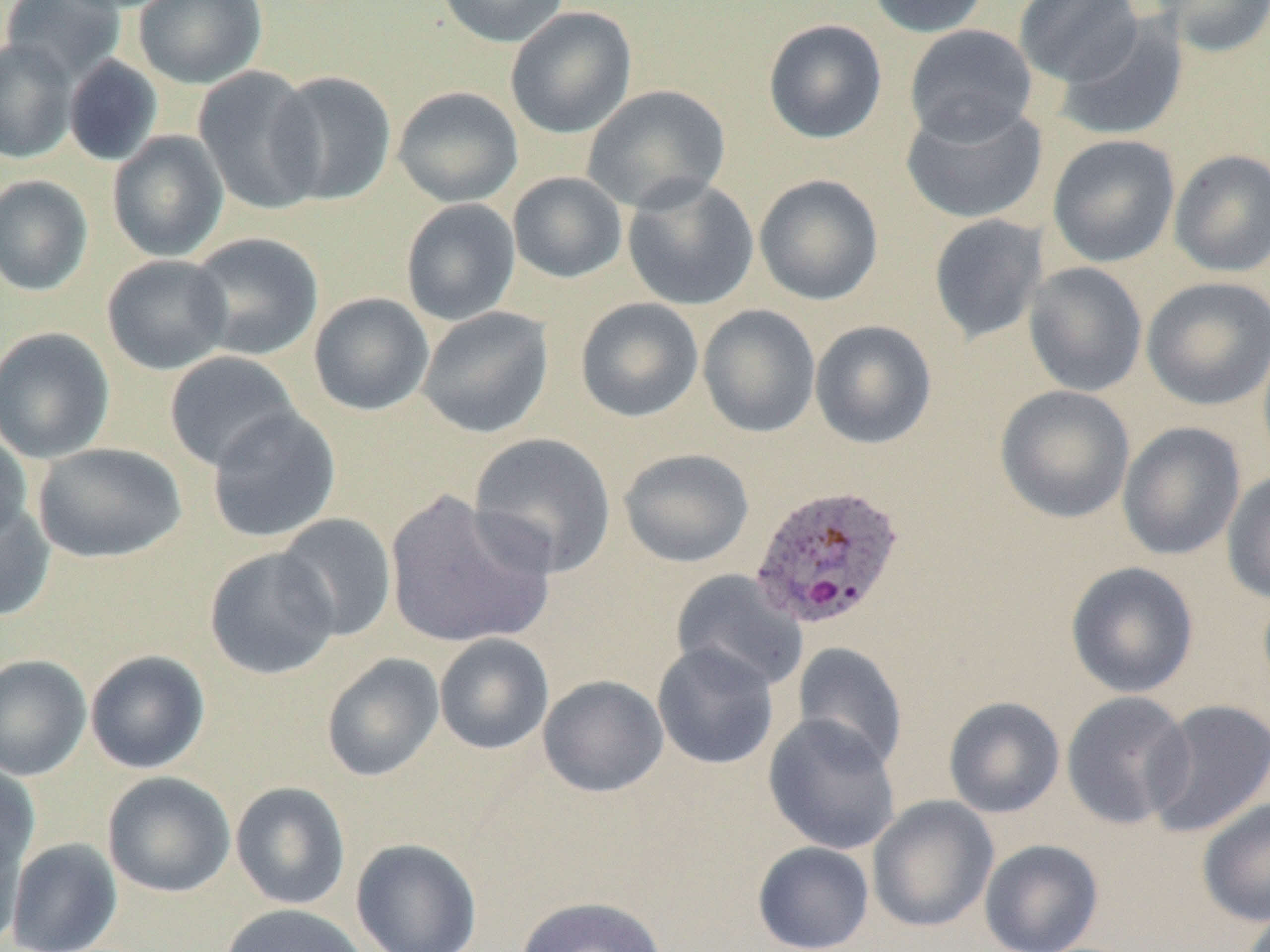
slide-level diagnosis = Plasmodium ovale
field of view = single
Plasmodium ovale-infected red blood cell locations = approximate bounding boxes as named x1/y1/x2/y2 corners in pixels: (x1=749, y1=482, x2=905, y2=632)
modality = light microscopy
magnification = 1000x
uninfected red blood cell locations = approximate bounding boxes as named x1/y1/x2/y2 corners in pixels: (x1=1, y1=0, x2=127, y2=84), (x1=133, y1=0, x2=268, y2=89), (x1=438, y1=0, x2=570, y2=48), (x1=866, y1=0, x2=992, y2=37), (x1=1014, y1=0, x2=1144, y2=87), (x1=1152, y1=0, x2=1270, y2=58), (x1=505, y1=6, x2=637, y2=139), (x1=1054, y1=16, x2=1189, y2=141), (x1=763, y1=18, x2=888, y2=144), (x1=904, y1=24, x2=1038, y2=145), (x1=0, y1=37, x2=78, y2=164), (x1=63, y1=55, x2=163, y2=167), (x1=194, y1=66, x2=326, y2=215), (x1=267, y1=71, x2=397, y2=207), (x1=582, y1=84, x2=731, y2=214), (x1=392, y1=86, x2=523, y2=208), (x1=901, y1=100, x2=1048, y2=225), (x1=107, y1=130, x2=229, y2=262), (x1=1047, y1=135, x2=1180, y2=268), (x1=1168, y1=148, x2=1270, y2=277), (x1=508, y1=172, x2=628, y2=283), (x1=754, y1=173, x2=884, y2=306), (x1=0, y1=175, x2=94, y2=296), (x1=622, y1=176, x2=759, y2=311), (x1=400, y1=199, x2=521, y2=327), (x1=928, y1=214, x2=1049, y2=345), (x1=186, y1=232, x2=324, y2=361), (x1=102, y1=254, x2=233, y2=375), (x1=1023, y1=262, x2=1148, y2=397), (x1=1140, y1=276, x2=1270, y2=410), (x1=308, y1=293, x2=434, y2=415), (x1=575, y1=297, x2=704, y2=423), (x1=697, y1=304, x2=821, y2=438), (x1=416, y1=306, x2=554, y2=439), (x1=809, y1=319, x2=937, y2=449), (x1=0, y1=327, x2=116, y2=464), (x1=163, y1=351, x2=302, y2=473), (x1=994, y1=385, x2=1136, y2=524), (x1=206, y1=407, x2=341, y2=543), (x1=1117, y1=421, x2=1246, y2=561), (x1=0, y1=426, x2=33, y2=546), (x1=469, y1=432, x2=617, y2=578), (x1=33, y1=442, x2=186, y2=563), (x1=619, y1=448, x2=754, y2=568), (x1=1221, y1=470, x2=1270, y2=604), (x1=384, y1=490, x2=556, y2=649), (x1=0, y1=498, x2=55, y2=622), (x1=274, y1=513, x2=397, y2=641), (x1=204, y1=546, x2=341, y2=680), (x1=1065, y1=561, x2=1199, y2=698), (x1=670, y1=569, x2=808, y2=692), (x1=434, y1=633, x2=554, y2=755), (x1=652, y1=642, x2=780, y2=770), (x1=791, y1=642, x2=908, y2=771), (x1=84, y1=650, x2=210, y2=774), (x1=321, y1=653, x2=445, y2=782), (x1=0, y1=654, x2=91, y2=780), (x1=538, y1=674, x2=668, y2=797), (x1=1061, y1=691, x2=1195, y2=829), (x1=943, y1=696, x2=1065, y2=818), (x1=1144, y1=699, x2=1270, y2=838), (x1=763, y1=713, x2=901, y2=855), (x1=0, y1=761, x2=41, y2=878), (x1=102, y1=771, x2=236, y2=898), (x1=230, y1=781, x2=351, y2=910), (x1=867, y1=796, x2=999, y2=933), (x1=1197, y1=797, x2=1270, y2=927), (x1=1, y1=817, x2=28, y2=950), (x1=6, y1=838, x2=122, y2=951), (x1=351, y1=838, x2=483, y2=952), (x1=979, y1=839, x2=1104, y2=951), (x1=752, y1=840, x2=875, y2=952), (x1=515, y1=896, x2=668, y2=952), (x1=219, y1=903, x2=370, y2=952)
preparation = thin blood smear
image size = 1270×952 pixels